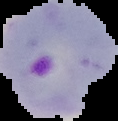
Summary:
  - Preparation: thin blood smear
  - Image type: cell region segmented out of the field of view; surrounding area masked to black
  - Malaria status: parasitized
  - Image size: 118×121 pixels